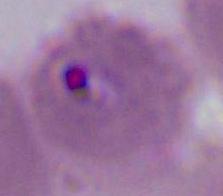

Summary:
  - Modality: photomicrograph
  - Magnification: 400x or 1000x
  - Identification: Plasmodium